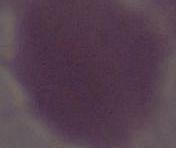
{
  "identification": "erythrocyte",
  "modality": "micrograph",
  "magnification": "1000x"
}